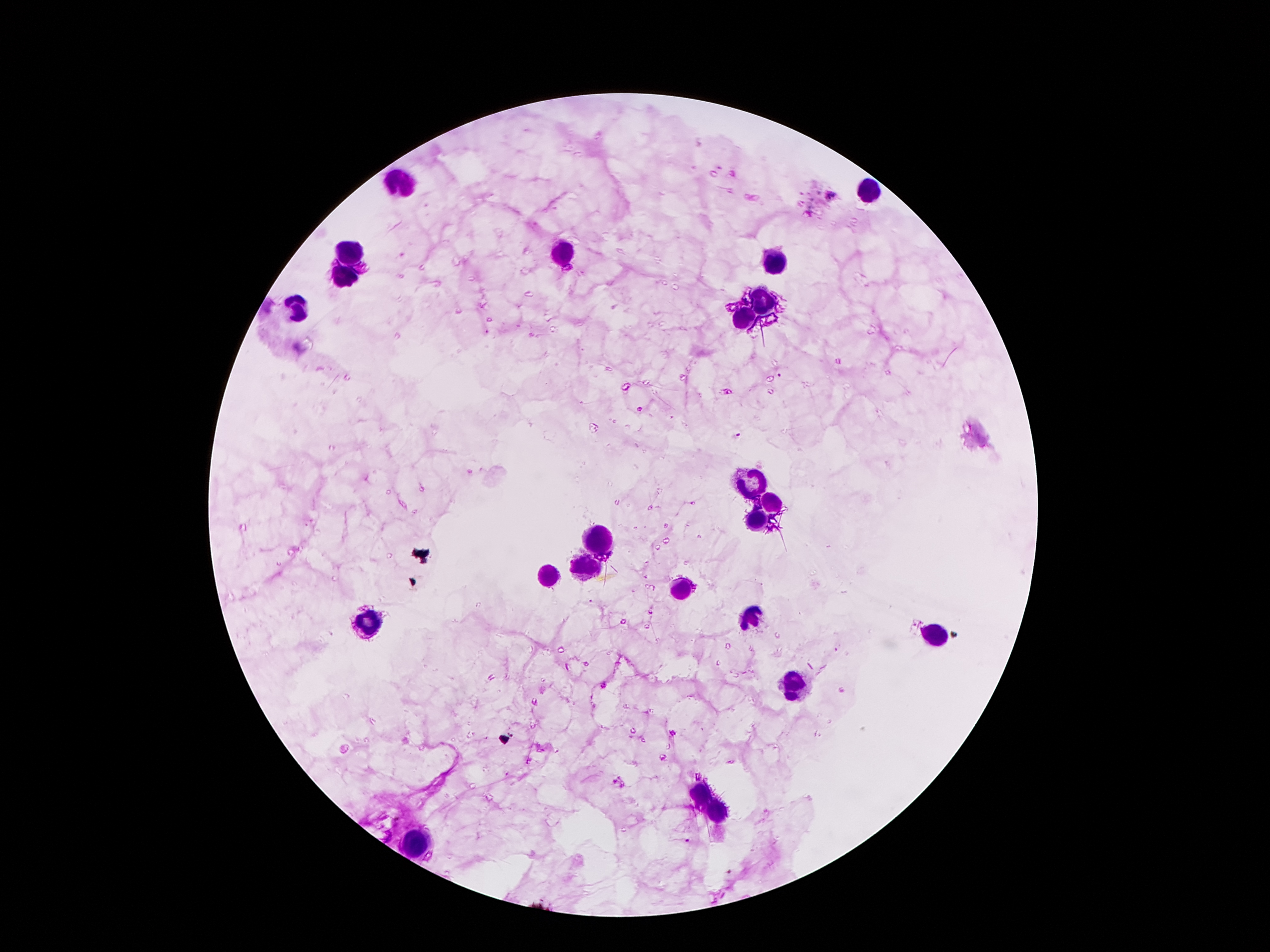
Approximate centers as {x, y} in pixels.
Summary:
  - Leukocyte locations: {402, 182}, {873, 194}, {351, 247}, {564, 253}, {775, 259}, {344, 280}, {765, 300}, {299, 309}, {744, 319}, {750, 481}, {771, 503}, {758, 522}, {599, 544}, {586, 565}, {549, 575}, {678, 589}, {750, 618}, {367, 624}, {937, 634}, {795, 686}, {697, 794}, {715, 813}, {412, 841}
  - Plasmodium parasite locations: {782, 375}, {639, 411}, {734, 435}, {685, 842}, {730, 871}
  - Magnification: 100x
  - Preparation: thick blood smear
  - Stain: Giemsa
  - Patient malaria status: positive for Plasmodium falciparum
  - Capture: smartphone camera through the microscope eyepiece
  - Field of view: one from this slide
  - Image size: 1270×952 pixels